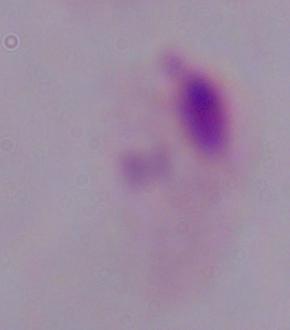

Captured at 1000x magnification. A trichomonad is shown. Micrograph.